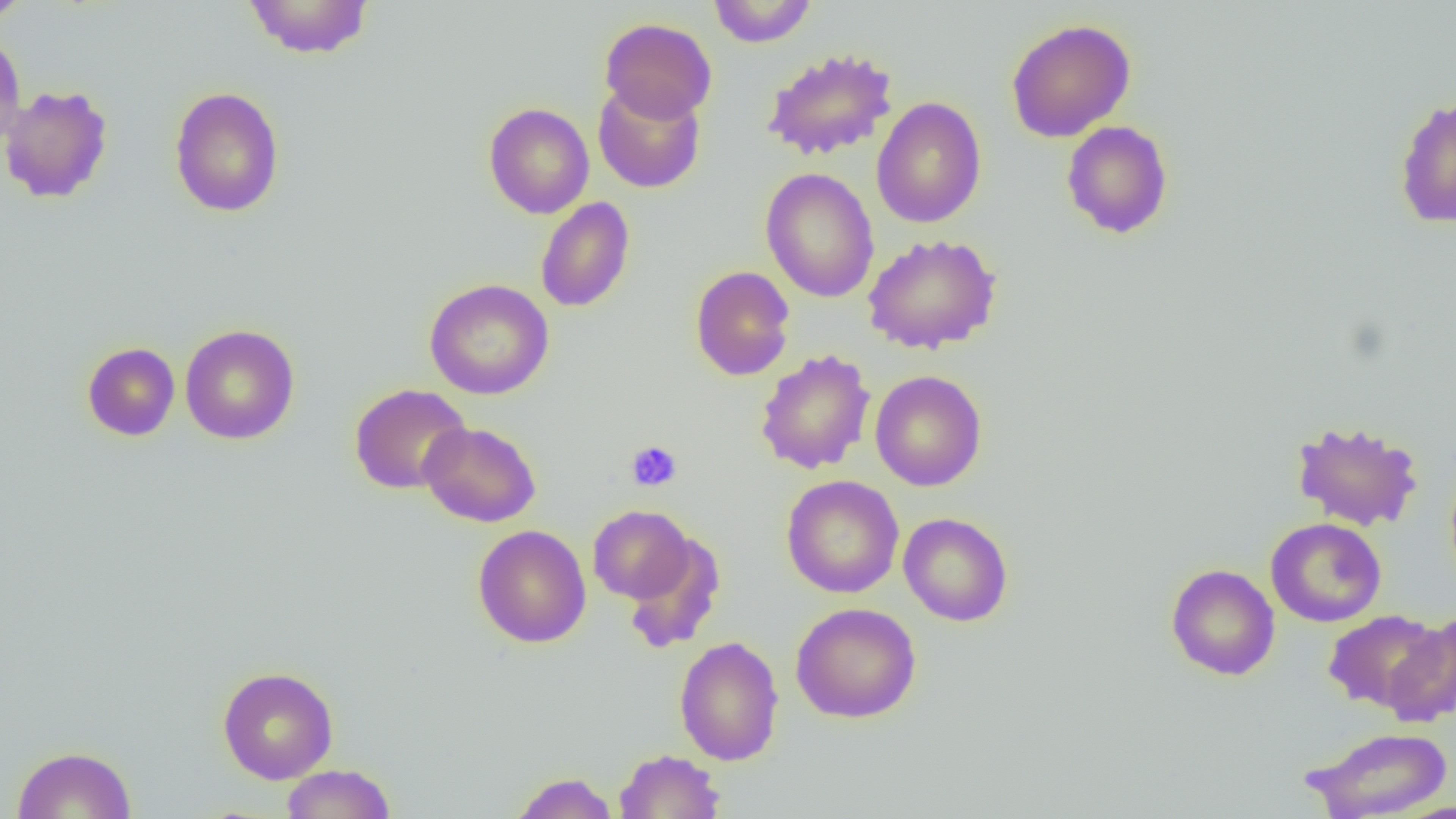
Summary:
  - Coordinate format: approximate bounding boxes as (x1,y1)-(x2,y2) corner pairs in pixels
  - Uninfected red blood cell locations: (0,0)-(34,24), (243,0)-(374,59), (708,0)-(818,47), (599,17)-(718,123), (1006,18)-(1136,142), (0,30)-(27,150), (761,47)-(899,162), (593,81)-(706,193), (0,84)-(114,204), (169,86)-(285,218), (1393,94)-(1456,229), (871,97)-(986,229), (483,103)-(594,219), (1061,120)-(1173,239), (760,167)-(880,303), (535,196)-(635,313), (862,233)-(1002,354), (690,265)-(795,381), (424,278)-(554,400), (180,324)-(300,444), (82,342)-(180,441), (755,349)-(876,475), (870,370)-(987,491), (349,383)-(472,494), (1291,419)-(1424,531), (418,421)-(541,527), (780,475)-(904,598), (587,505)-(694,604), (898,512)-(1014,627), (1266,518)-(1386,627), (473,524)-(592,648), (622,533)-(726,654), (1166,563)-(1280,680), (790,602)-(922,724), (1323,610)-(1446,713), (1382,615)-(1456,725), (674,635)-(785,766), (217,666)-(338,784), (1305,726)-(1452,819), (12,746)-(138,818), (614,749)-(725,818), (280,763)-(397,819), (509,771)-(619,818)
  - Platelet locations: (626,441)-(682,491)
  - Slide-level diagnosis: negative for blood parasites
  - Image size: 1456×819 pixels
  - Modality: light microscopy
  - Magnification: 1000x
  - Field of view: single
  - Preparation: thin blood smear